Classify this cell by malaria status.
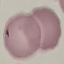
Uninfected.

Cell patch, automatically extracted from a larger field of view and resized to 64 × 64 pixels. Acquired by smartphone through the microscope eyepiece. Giemsa-stained preparation. Thin smear of blood.